Give the position of every leukocyte visible.
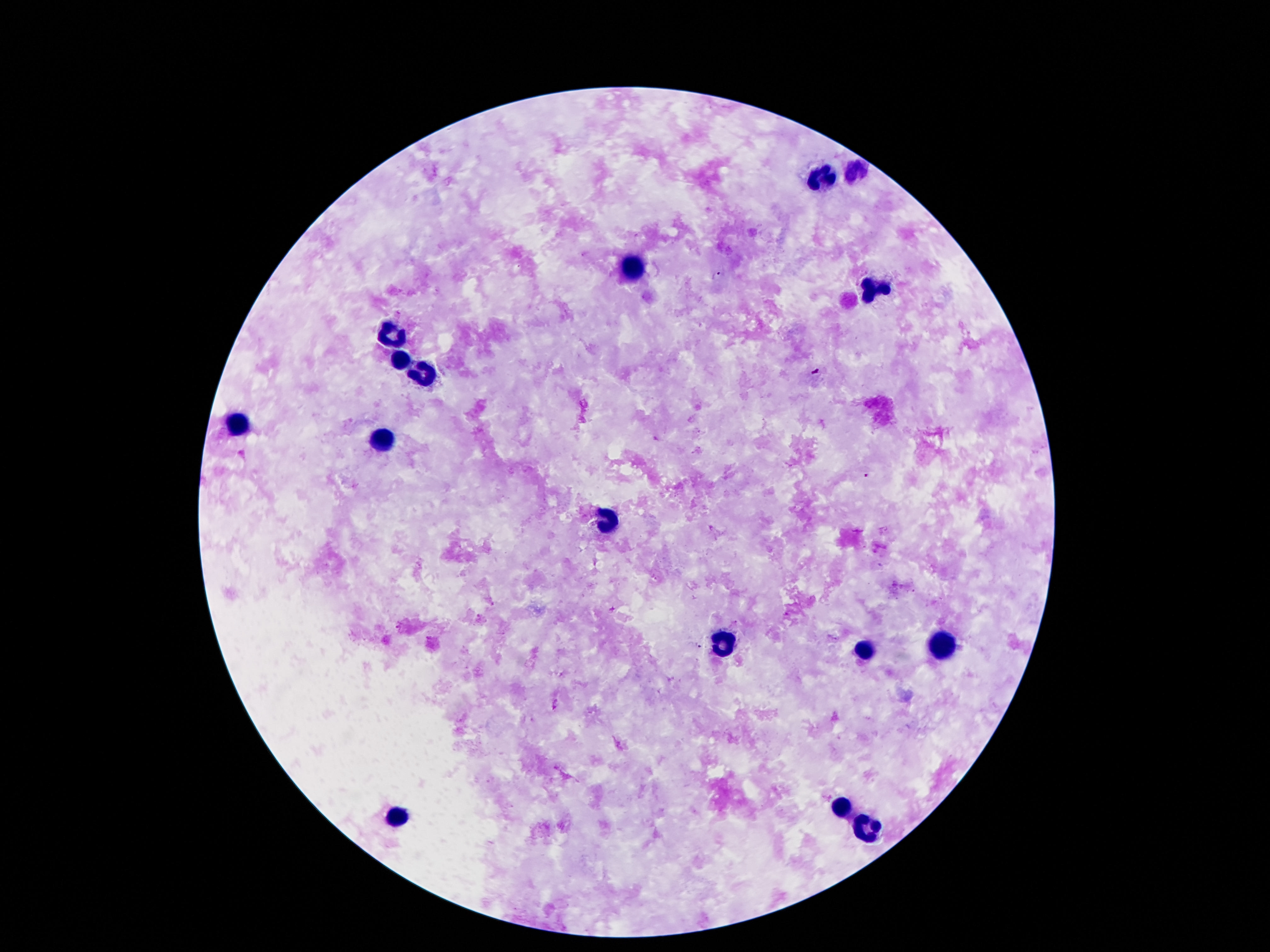

Approximate centers as (x, y) in pixels.
Leukocytes: (855, 172), (819, 178), (630, 265), (876, 290), (391, 336), (399, 362), (426, 376), (242, 426), (382, 441), (609, 523), (725, 644), (939, 647), (863, 651), (842, 806), (397, 817), (867, 830).

Patient malaria status: not infected. Image is 1270×952 pixels. Giemsa stain. Smartphone photograph taken through the microscope eyepiece. 100x magnification. One field from this slide. Thick blood smear.